Assess the background quality.
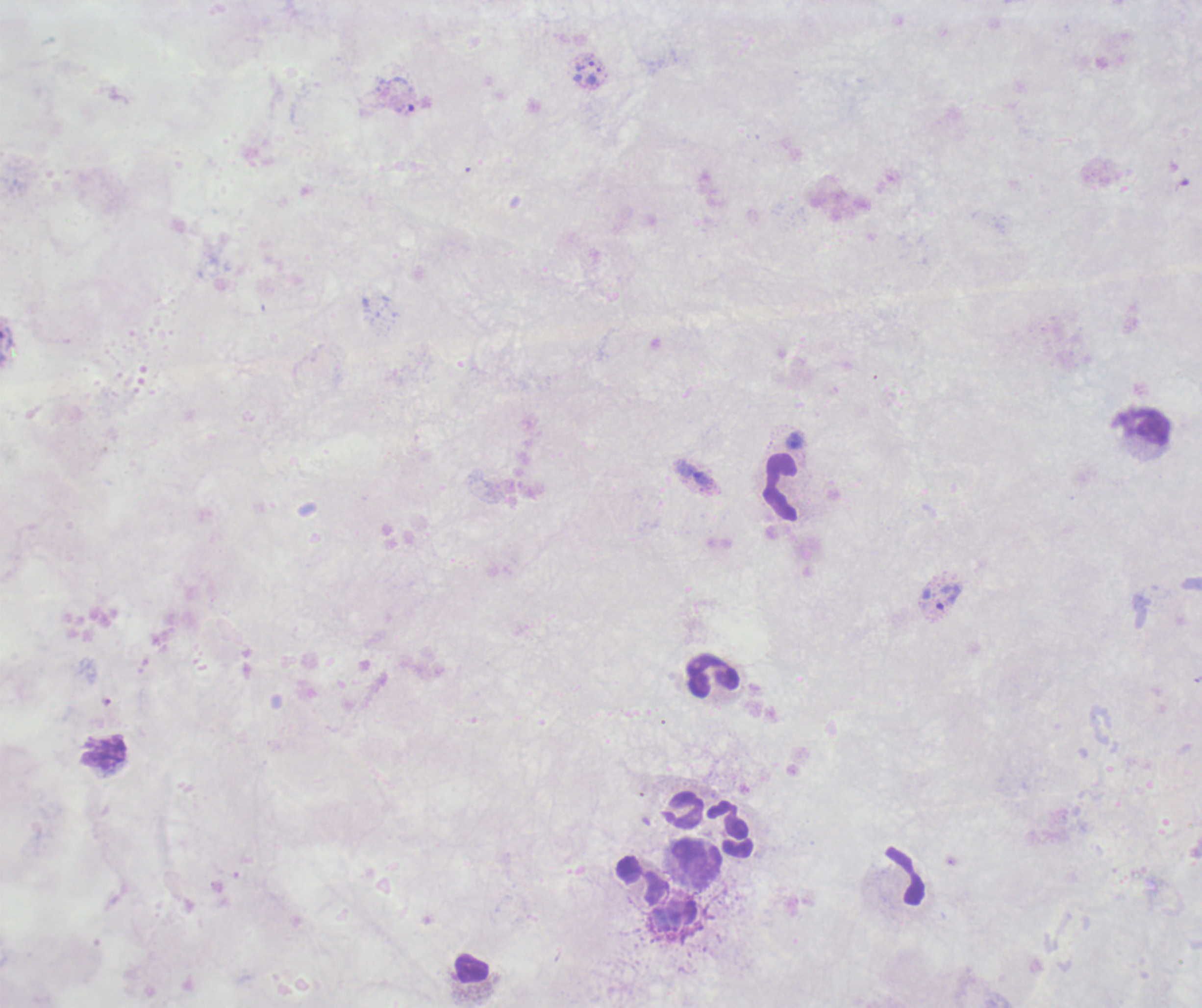
Poor.

{
  "magnification": "100x",
  "stain": "Romanowsky",
  "leukocyte_locations": "approximate object centers, in pixels from the top-left corner: (x=1140, y=425), (x=780, y=487), (x=713, y=675), (x=103, y=753), (x=684, y=809), (x=731, y=829), (x=697, y=863), (x=905, y=874), (x=640, y=881), (x=471, y=967)",
  "field_of_view": "one from this slide",
  "image_size": "1202×1008 pixels",
  "coloration_quality": "bad",
  "result": "malaria parasites identified",
  "trophozoite_locations": "approximate object centers, in pixels from the top-left corner: (x=594, y=76), (x=404, y=109), (x=693, y=473), (x=941, y=597)",
  "preparation": "thick smear of blood",
  "context": "previously used in an actual diagnosis"
}